Report the malaria status of this cell.
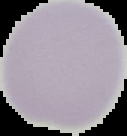

Uninfected.

Summary:
  - Image type: segmented cell region on a black background
  - Image size: 127×136 pixels
  - Preparation: thin blood film